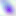
Micrograph. 400x magnification. Toxoplasma gondii is seen.